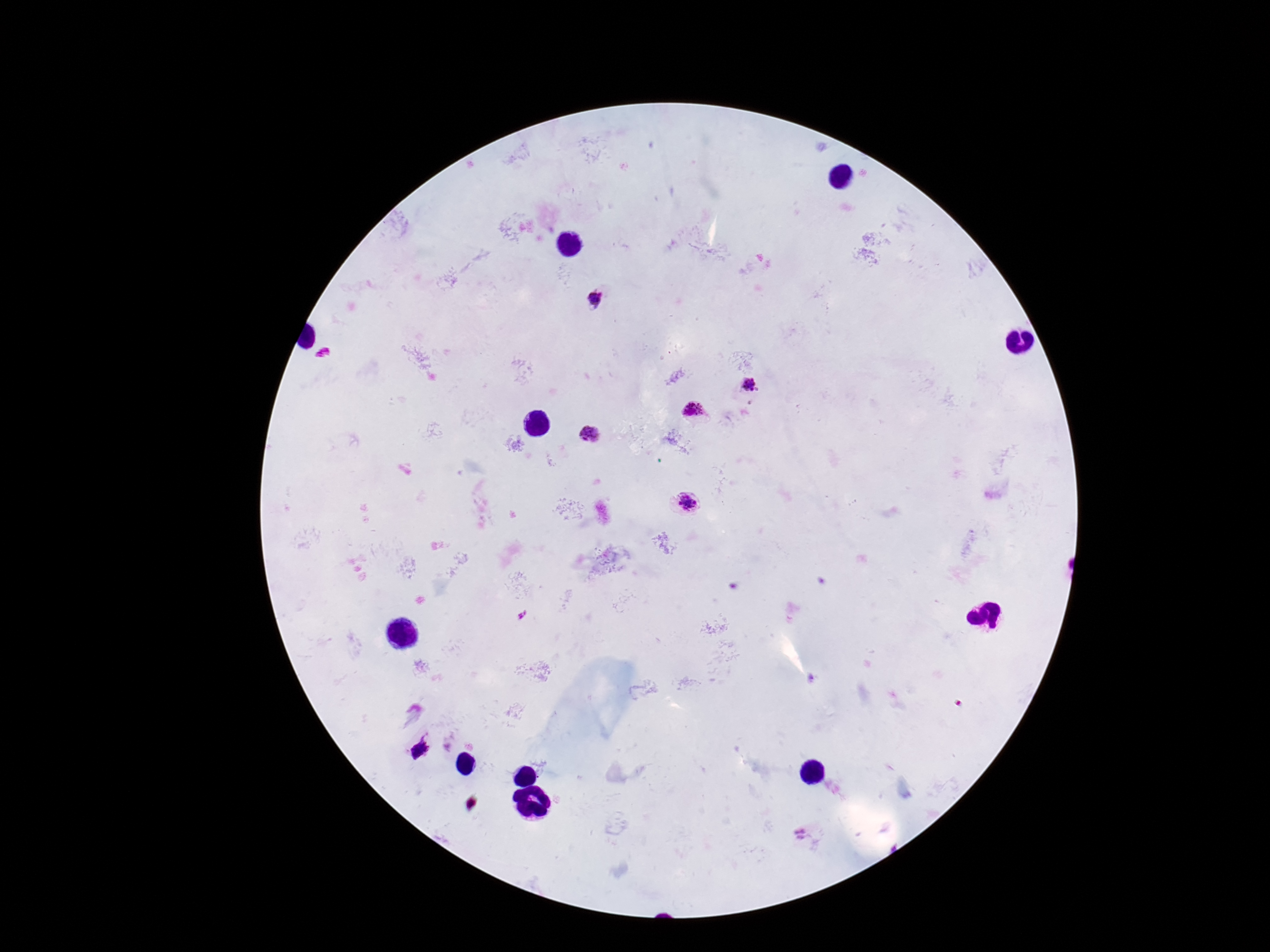
preparation = thick blood film
patient malaria status = positive
stain = Giemsa
magnification = 100x
field of view = single
image size = 1270×952 pixels
capture = smartphone camera through the microscope eyepiece
Plasmodium parasite locations = approximate centers as (x, y) in pixels: (594, 298), (323, 355), (749, 385), (695, 411), (591, 434), (687, 504), (420, 749)